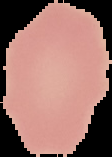
Summary:
  - Image size: 112×157 pixels
  - Image type: segmented cell region with the area outside set to black
  - Preparation: thin blood smear
  - Malaria status: uninfected